Locate every Trypanosoma brucei.
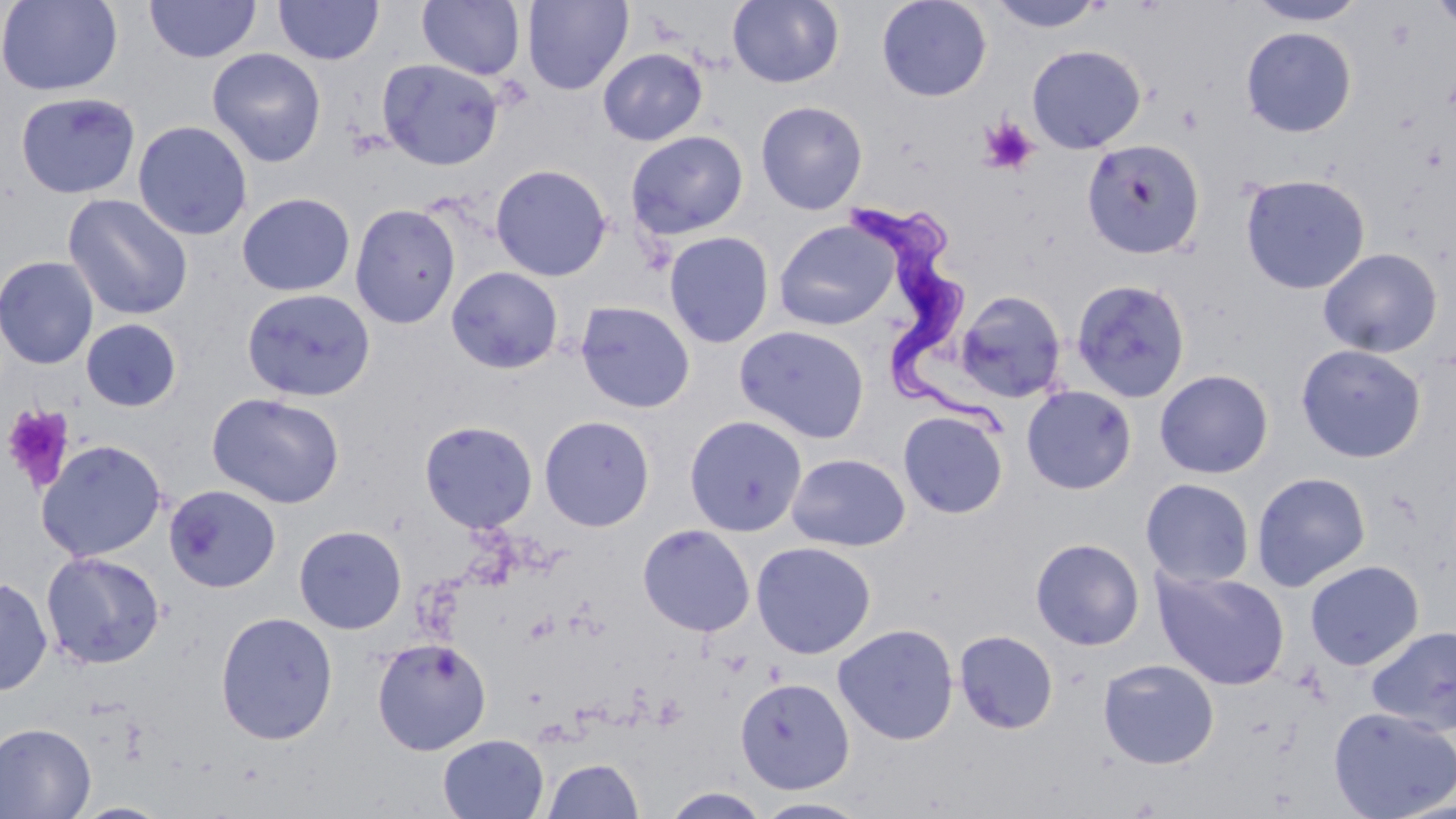
Approximate bounding boxes as (x1,y1)-(x2,y2) corner pairs in pixels.
Trypanosoma brucei: (853,203)-(1011,443).

Uninfected red blood cell locations: (0,0)-(123,96), (145,0)-(261,63), (273,0)-(384,65), (417,0)-(526,80), (522,0)-(634,95), (727,0)-(844,89), (876,0)-(992,102), (986,0)-(1108,33), (1244,0)-(1371,26), (1427,0)-(1456,34), (1240,26)-(1357,137), (1026,44)-(1146,153), (207,48)-(327,167), (597,48)-(708,146), (376,58)-(504,171), (15,92)-(141,199), (755,100)-(869,214), (132,120)-(253,241), (625,130)-(749,241), (1081,139)-(1205,259), (490,163)-(613,282), (1239,173)-(1371,294), (236,192)-(355,296), (62,193)-(194,321), (349,203)-(461,329), (773,220)-(899,331), (663,231)-(775,348), (1318,247)-(1443,358), (0,256)-(99,370), (446,266)-(563,374), (1071,278)-(1193,403), (241,288)-(376,402), (955,289)-(1067,403), (575,300)-(696,414), (80,318)-(183,412), (734,324)-(870,443), (1295,343)-(1427,463), (1154,369)-(1274,479), (1021,385)-(1138,495), (206,392)-(345,509), (897,410)-(1009,519), (683,413)-(808,536), (538,414)-(655,531), (419,420)-(538,533), (36,439)-(168,562), (786,452)-(910,552), (1251,471)-(1372,591), (1140,478)-(1255,589), (164,484)-(281,593), (637,523)-(756,637), (293,525)-(407,634), (1030,538)-(1145,651), (751,540)-(877,659), (40,550)-(166,670), (1304,559)-(1424,670), (1152,567)-(1290,689), (0,574)-(53,697), (214,611)-(339,745), (832,623)-(960,745), (1366,625)-(1456,736), (953,629)-(1059,734), (371,636)-(492,756), (1097,659)-(1220,769), (734,677)-(854,793), (1328,706)-(1456,819), (0,721)-(96,819), (437,733)-(550,818), (541,757)-(644,818), (660,787)-(773,818), (753,797)-(872,818), (71,802)-(174,819). Platelet locations: (978,117)-(1039,175), (1,403)-(76,493). Slide-level diagnosis: Trypanosoma brucei. One field of a larger specimen. Optical microscopy. Image is 1456×819 pixels. Captured at 1000x magnification. May-Grünwald-Giemsa-stained preparation. Thin blood smear.